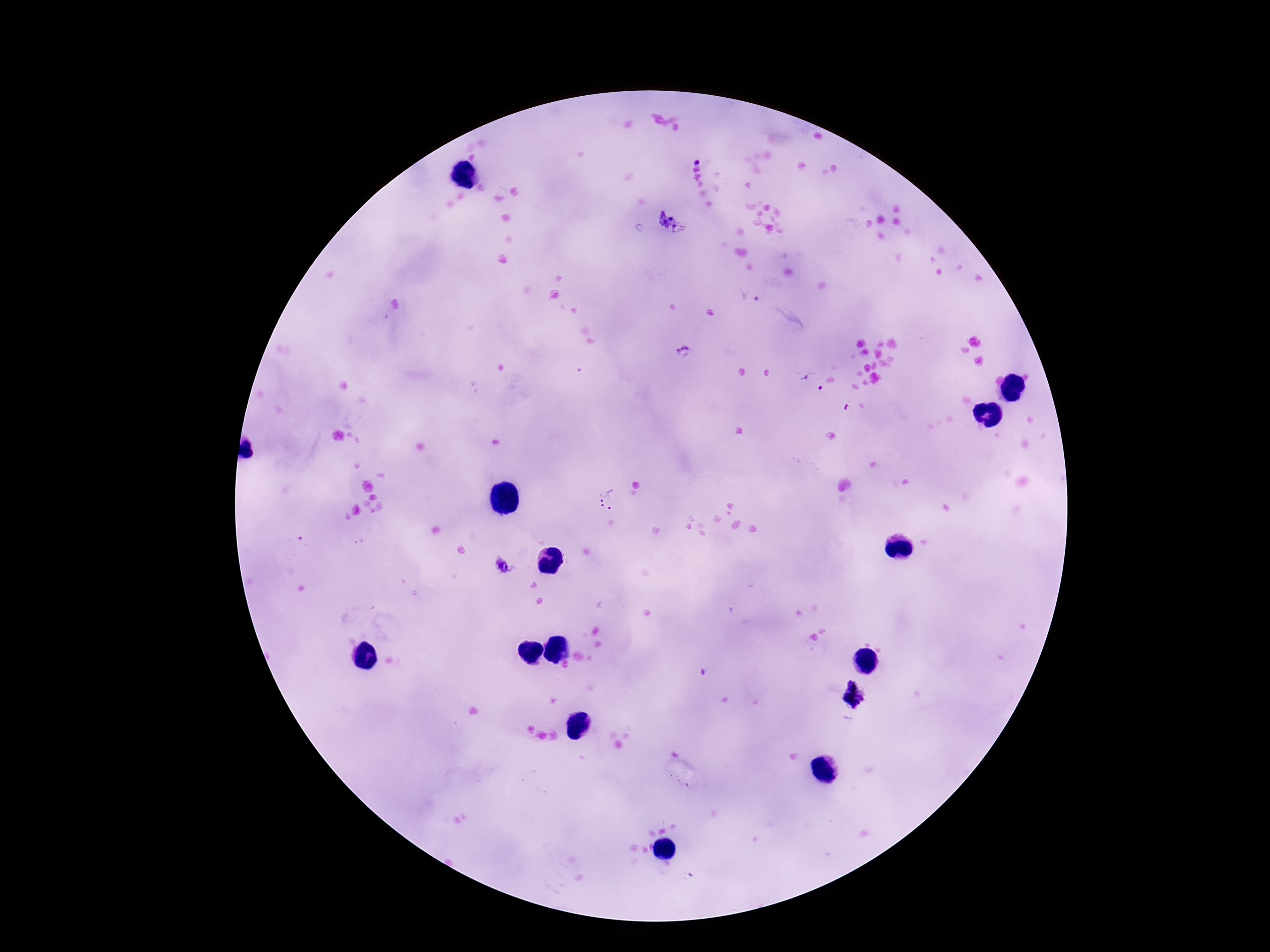

stain = Giemsa
field of view = single
image size = 1270×952 pixels
Plasmodium parasite locations = approximate object centers, in pixels from the top-left corner: (x=697, y=160), (x=671, y=222), (x=750, y=296), (x=684, y=352), (x=812, y=382), (x=607, y=499), (x=506, y=564), (x=856, y=695)
preparation = thick blood film
patient malaria status = infected
capture = smartphone camera through the microscope eyepiece
magnification = 100x